Name the parasite shown.
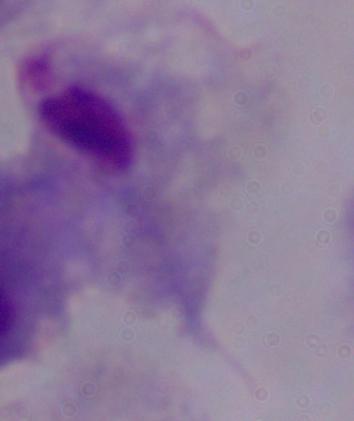
This is a trichomonad.

Summary:
  - Magnification: 1000x
  - Modality: micrograph